Classify this cell by malaria status.
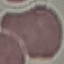

It is uninfected.

Photographed with a smartphone camera at the microscope eyepiece. Automatically extracted cell patch, resized to 64 × 64 pixels. Thin blood smear. Giemsa-stained preparation.